Identify the parasite.
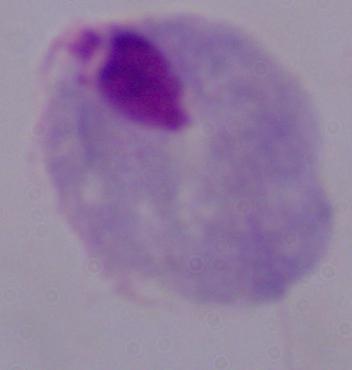
A trichomonad.

magnification = 1000x
modality = photomicrograph